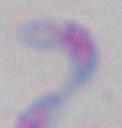
magnification = 1000x
identification = Toxoplasma gondii
modality = micrograph